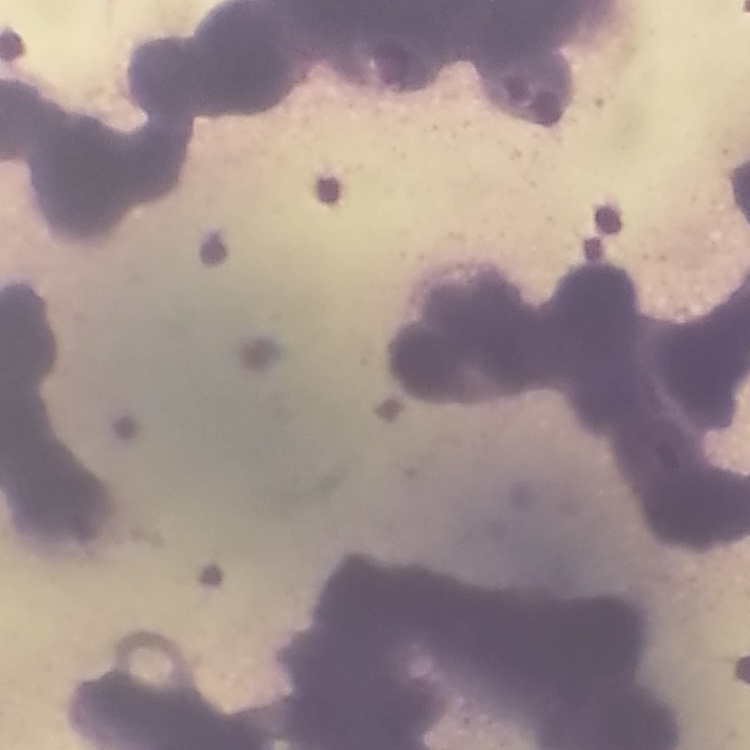

erythrocyte morphology = rouleaux formation
preparation = thin peripheral smear
stain = Field's or Giemsa
image type = square crop of a larger photomicrograph